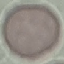 Result: no malaria parasites seen. Thin smear of blood. Giemsa stain. Cell patch, automatically extracted from a larger field of view and resized to 64 × 64 pixels. Photographed with a smartphone camera at the microscope eyepiece.